State the preparation type.
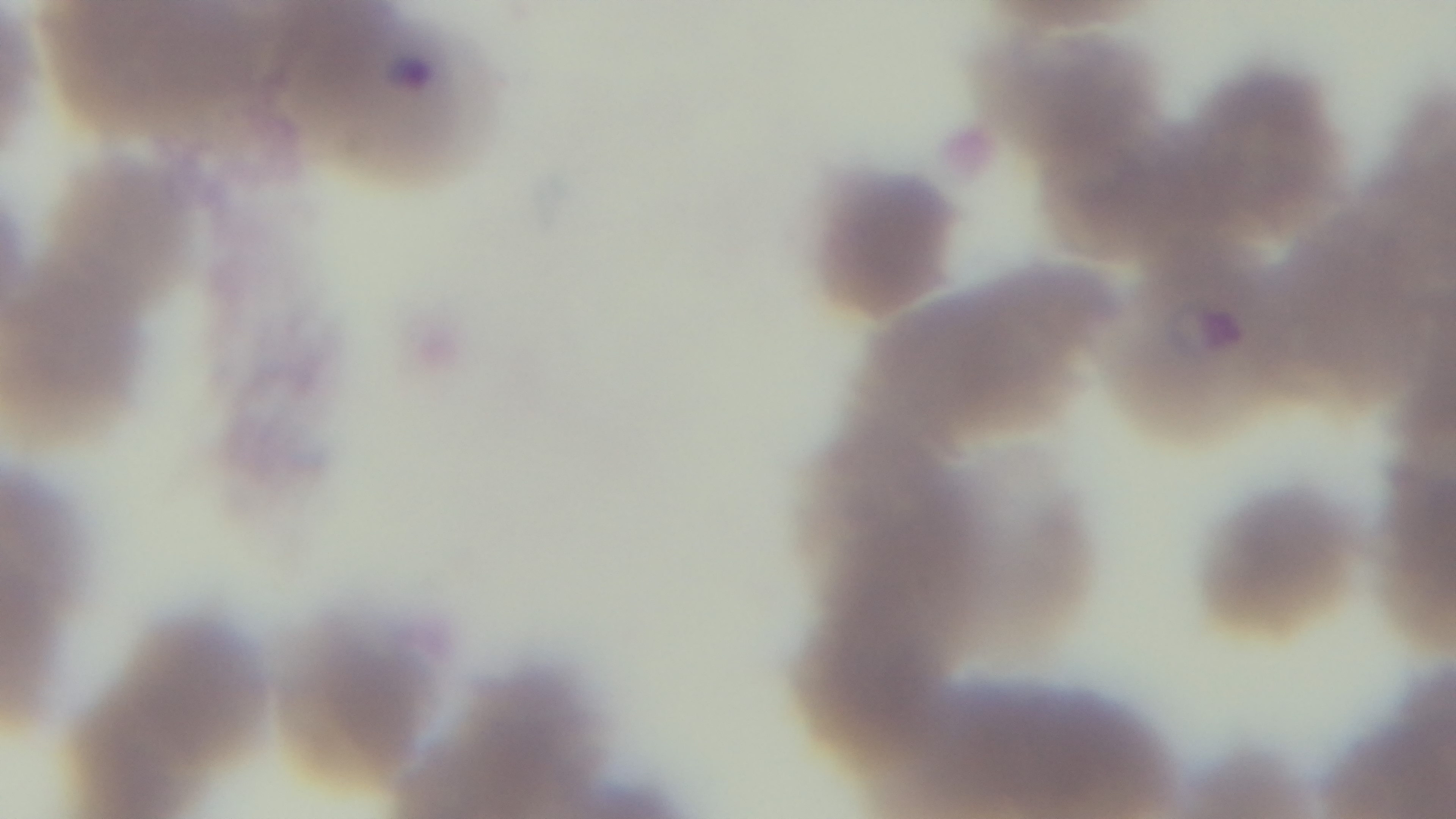

It is a thin blood film.

capture = mounted 4K digital camera
modality = light microscopy
field of view = single
stain = Giemsa
malaria status = infected
objective = 100x oil immersion